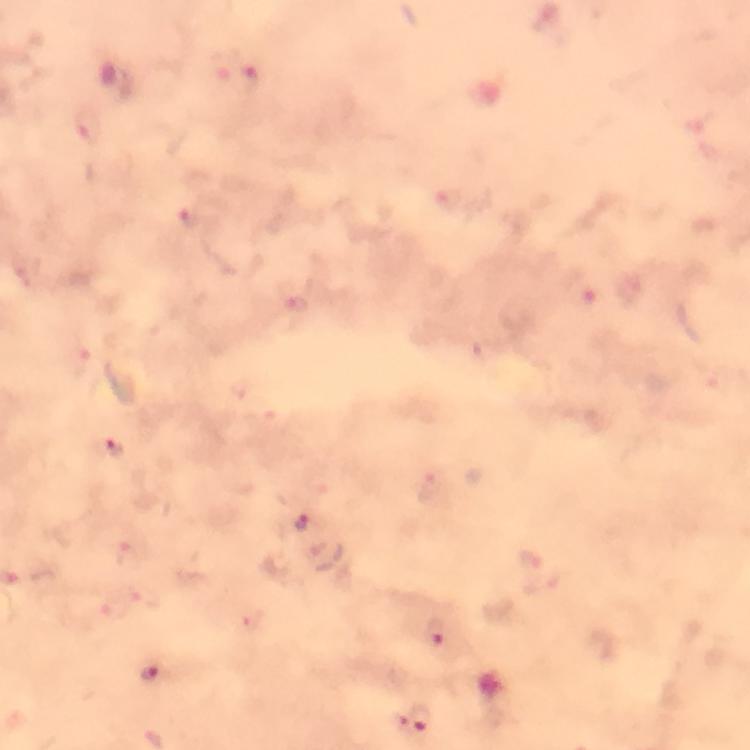
Approximate object centers, in pixels from the top-left corner.
Summary:
  - Plasmodium parasite locations: (x=249, y=80), (x=89, y=130), (x=450, y=199), (x=190, y=216), (x=577, y=289), (x=301, y=305), (x=81, y=362), (x=116, y=449), (x=431, y=488), (x=300, y=522), (x=144, y=593), (x=112, y=606), (x=438, y=634), (x=150, y=674), (x=422, y=717), (x=401, y=722)
  - Capture: smartphone camera through the microscope
  - Immersion oil: applied
  - Magnification: 100x
  - Context: from a malaria diagnostic workup
  - Image size: 750×750 pixels
  - Preparation: thick blood film
  - Cropped from: a single field of view
  - Stain: Giemsa